Classify this cell by malaria status.
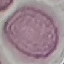
It is uninfected.

Summary:
  - Preparation: thin blood smear
  - Image type: automatically extracted cell patch, resized to 64 × 64 pixels
  - Capture: smartphone through the microscope eyepiece
  - Stain: Giemsa